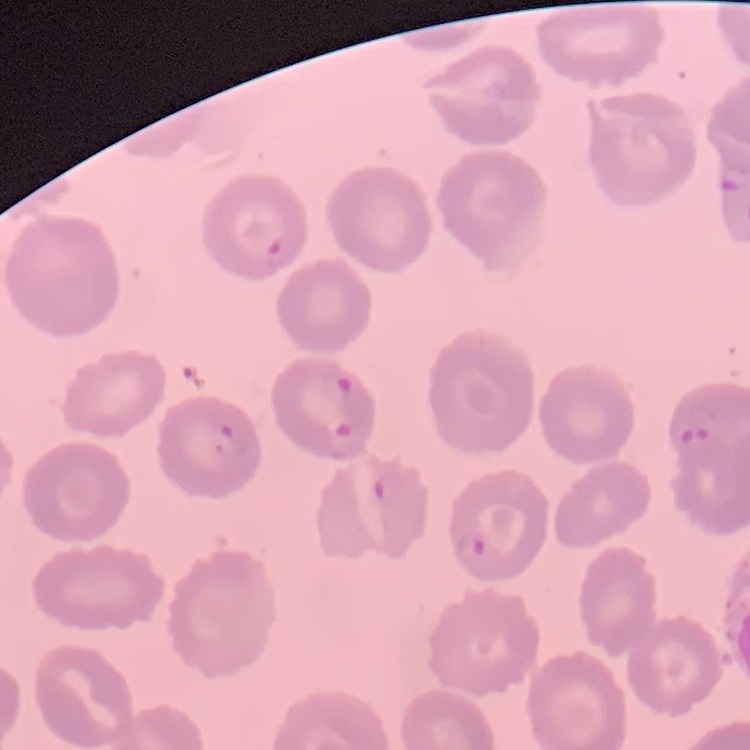
Summary:
  - Erythrocyte morphology: no rouleaux formation
  - Stain: Field's or Giemsa
  - Preparation: thin blood smear
  - Image type: square crop of a larger photomicrograph